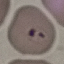 Result: malaria parasites detected. Photographed with a smartphone camera at the microscope eyepiece. Thin smear of blood. Giemsa-stained preparation. Automatically extracted cell patch, resized to 64 × 64 pixels.